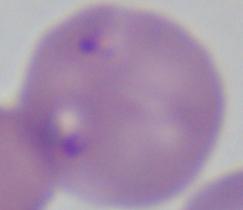
Summary:
  - Magnification: 1000x
  - Modality: photomicrograph
  - Identification: Babesia